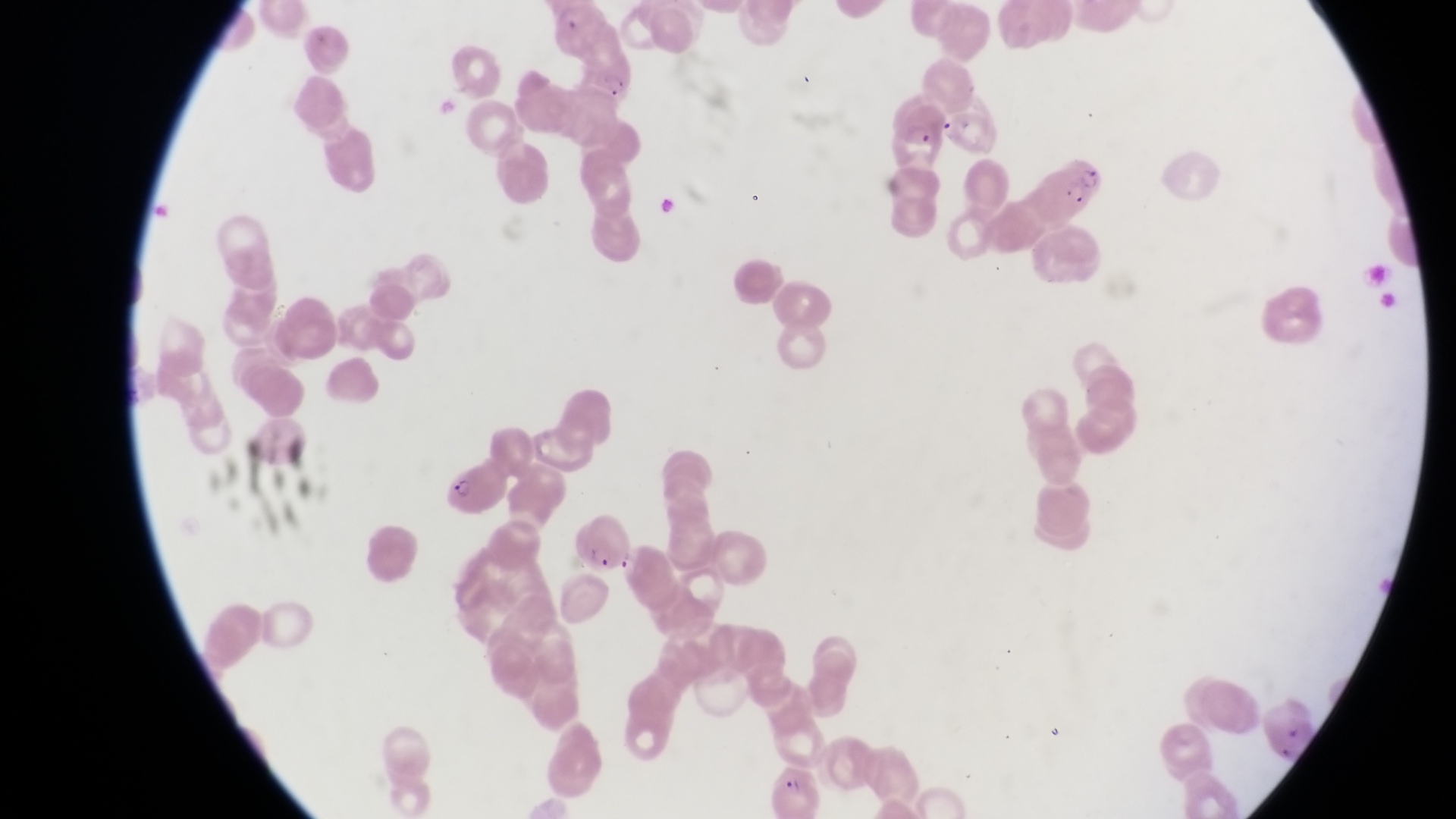

Approximate bounding boxes as (left, top, right, bottom) in pixels.
Summary:
  - Parasitised red blood cell locations: (547, 5, 602, 42), (891, 100, 949, 160), (1036, 146, 1110, 217), (435, 462, 508, 518), (570, 513, 631, 574), (767, 767, 822, 819)
  - Capture: smartphone photograph through the eyepiece of an Olympus CX-23 microscope
  - Field of view: single
  - Preparation: thin blood smear
  - Image size: 1456×819 pixels
  - Country: Uganda
  - Magnification: 1000x